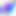

400x magnification. Micrograph. Toxoplasma gondii is seen.